Identify the blood parasite species.
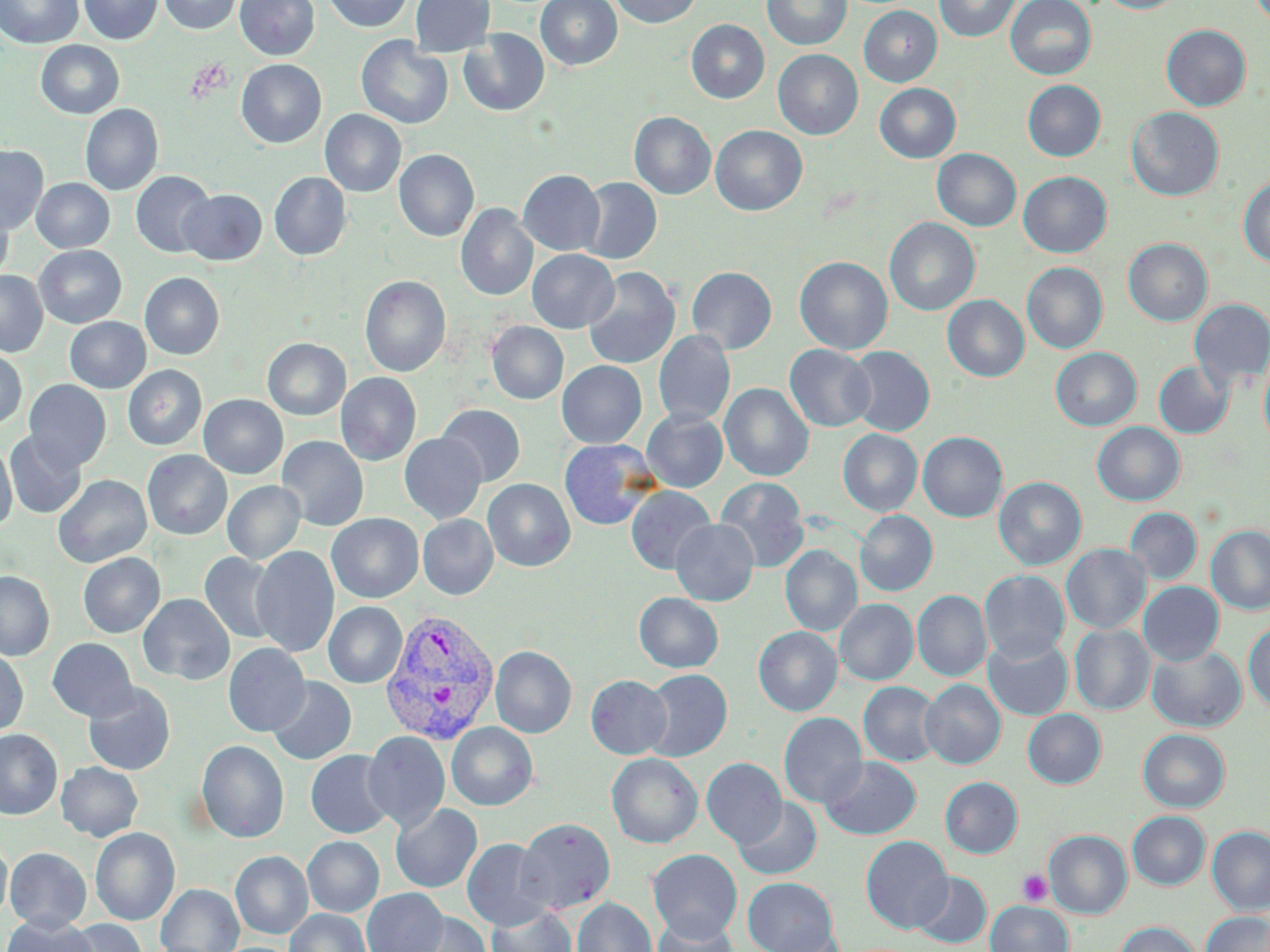
Plasmodium vivax.

Summary:
  - Coordinate format: approximate bounding boxes as (x1,y1)-(x2,y2) corner pairs in pixels
  - Plasmodium vivax-infected red blood cell locations: (379,609)-(500,747)
  - Uninfected red blood cell locations: (0,0)-(84,49), (78,0)-(162,44), (159,0)-(241,34), (235,0)-(319,60), (324,0)-(413,32), (410,0)-(495,56), (535,0)-(622,70), (611,0)-(702,28), (762,0)-(851,51), (934,0)-(1021,42), (1005,0)-(1097,80), (1097,0)-(1185,13), (859,5)-(942,87), (686,19)-(769,103), (1161,24)-(1251,111), (459,29)-(549,117), (356,37)-(453,129), (35,40)-(124,119), (773,49)-(862,140), (236,59)-(326,148), (1023,80)-(1105,161), (874,83)-(961,163), (80,104)-(162,196), (1126,107)-(1224,201), (320,109)-(406,197), (629,112)-(715,200), (710,125)-(807,216), (0,145)-(48,235), (394,149)-(479,242), (932,149)-(1021,231), (518,169)-(605,256), (131,171)-(216,258), (1018,171)-(1112,257), (269,172)-(351,261), (1238,176)-(1270,268), (578,177)-(661,264), (31,178)-(114,252), (179,189)-(267,265), (0,200)-(14,285), (456,204)-(538,301), (884,217)-(980,316), (1123,238)-(1212,326), (34,245)-(126,328), (527,249)-(619,333), (794,256)-(893,354), (1022,262)-(1107,354), (686,266)-(777,354), (582,268)-(680,369), (0,270)-(48,357), (140,272)-(224,359), (359,275)-(451,377), (942,295)-(1029,381), (1188,298)-(1270,390), (65,317)-(150,393), (487,321)-(568,404), (653,330)-(735,427), (263,338)-(350,420), (784,345)-(875,432), (845,346)-(935,436), (1050,347)-(1141,431), (0,348)-(27,429), (1259,351)-(1270,451), (557,360)-(647,448), (1153,361)-(1234,438), (123,365)-(207,450), (336,373)-(421,466), (24,380)-(111,471), (719,382)-(813,482), (199,394)-(288,478), (436,404)-(525,487), (642,408)-(728,492), (1092,422)-(1185,506), (838,429)-(922,516), (4,430)-(87,518), (918,432)-(1007,522), (399,433)-(486,524), (276,435)-(368,532), (0,438)-(17,533), (559,439)-(659,530), (142,450)-(232,540), (53,474)-(151,567), (994,476)-(1086,570), (715,477)-(809,573), (482,479)-(575,572), (222,480)-(305,564), (626,485)-(716,574), (1125,506)-(1202,584), (855,510)-(938,596), (326,513)-(423,603), (417,515)-(498,599), (670,518)-(759,606), (1206,525)-(1270,615), (1061,544)-(1151,633), (250,545)-(339,658), (780,545)-(862,637), (77,552)-(165,638), (199,552)-(282,644), (979,570)-(1069,663), (0,571)-(54,660), (1138,582)-(1224,666), (912,590)-(992,682), (634,592)-(723,673), (138,593)-(234,686), (834,599)-(918,685), (323,602)-(407,688), (1244,620)-(1270,714), (1070,625)-(1155,715), (753,626)-(843,716), (983,636)-(1073,720), (47,638)-(137,721), (223,643)-(310,736), (491,646)-(576,738), (1147,646)-(1246,732), (0,649)-(28,737), (641,669)-(732,762), (586,675)-(672,759), (267,677)-(356,765), (920,679)-(1005,769), (859,681)-(943,767), (82,682)-(176,776), (1023,709)-(1106,788), (779,712)-(867,809), (446,722)-(537,810), (1138,728)-(1230,812), (0,729)-(62,819), (363,731)-(449,831), (196,740)-(289,843), (305,750)-(396,839), (606,753)-(702,848), (821,757)-(921,840), (701,758)-(787,848), (56,761)-(143,841), (940,776)-(1023,858), (733,797)-(823,880), (391,803)-(482,893), (1127,811)-(1210,890), (517,817)-(616,914), (1208,826)-(1270,915), (90,827)-(180,925), (1044,830)-(1132,918), (861,835)-(953,934), (303,836)-(384,917), (0,837)-(12,923), (461,838)-(553,931), (4,847)-(91,932), (648,849)-(742,941), (231,851)-(313,939), (912,872)-(991,949), (743,877)-(838,952), (156,884)-(244,952), (362,888)-(448,952), (572,898)-(656,952), (986,901)-(1073,952), (485,902)-(576,952), (285,909)-(372,952), (402,911)-(491,951), (1202,912)-(1270,952), (652,915)-(739,952), (0,916)-(98,952), (63,919)-(147,952), (1115,921)-(1202,952), (764,926)-(846,952)
  - Platelet locations: (1018,870)-(1052,906)
  - Magnification: 1000x
  - Modality: optical microscopy
  - Image size: 1270×952 pixels
  - Preparation: thin blood smear
  - Stain: May-Grünwald-Giemsa
  - Field of view: single